Outline each blood parasite and name the species.
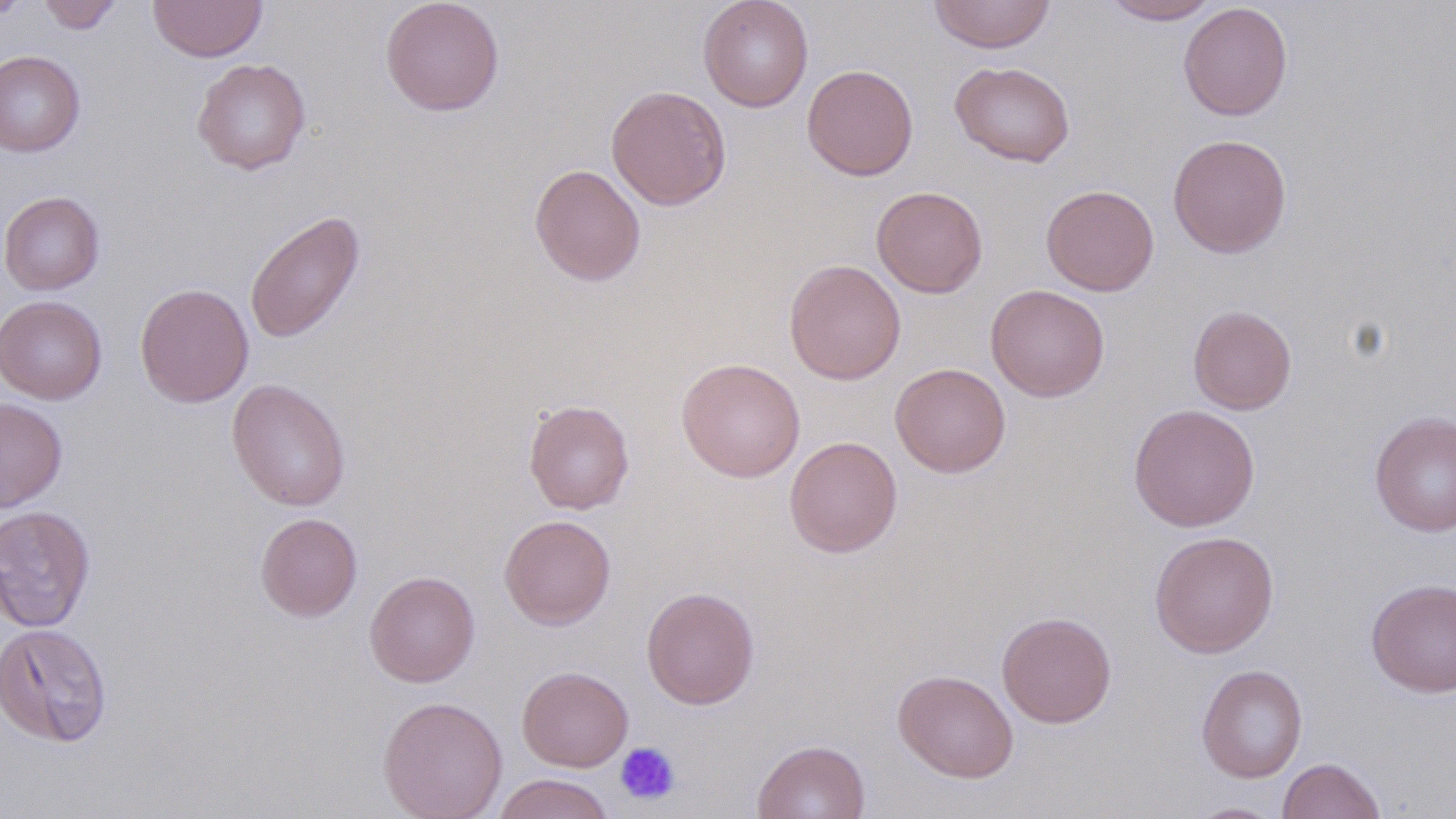

No blood parasites observed.

Approximate bounding boxes as named x1/y1/x2/y2 corners in pixels. Uninfected red blood cell locations: (x1=37, y1=0, x2=123, y2=33), (x1=149, y1=0, x2=267, y2=62), (x1=380, y1=0, x2=505, y2=116), (x1=697, y1=0, x2=814, y2=112), (x1=927, y1=0, x2=1056, y2=54), (x1=1101, y1=0, x2=1222, y2=24), (x1=1178, y1=3, x2=1294, y2=121), (x1=0, y1=51, x2=85, y2=157), (x1=192, y1=57, x2=311, y2=175), (x1=950, y1=61, x2=1076, y2=167), (x1=801, y1=64, x2=919, y2=181), (x1=605, y1=85, x2=732, y2=211), (x1=1167, y1=133, x2=1292, y2=258), (x1=530, y1=163, x2=646, y2=286), (x1=1041, y1=184, x2=1159, y2=296), (x1=871, y1=186, x2=988, y2=298), (x1=0, y1=191, x2=105, y2=295), (x1=244, y1=210, x2=365, y2=344), (x1=784, y1=259, x2=906, y2=385), (x1=134, y1=283, x2=254, y2=408), (x1=985, y1=284, x2=1110, y2=402), (x1=0, y1=294, x2=107, y2=404), (x1=1188, y1=304, x2=1297, y2=415), (x1=676, y1=357, x2=806, y2=482), (x1=890, y1=362, x2=1011, y2=478), (x1=227, y1=379, x2=351, y2=512), (x1=0, y1=397, x2=68, y2=512), (x1=523, y1=399, x2=634, y2=514), (x1=1128, y1=403, x2=1260, y2=531), (x1=1369, y1=410, x2=1456, y2=537), (x1=785, y1=435, x2=903, y2=558), (x1=0, y1=505, x2=96, y2=633), (x1=255, y1=512, x2=362, y2=622), (x1=499, y1=515, x2=616, y2=630), (x1=1149, y1=530, x2=1279, y2=658), (x1=364, y1=570, x2=480, y2=687), (x1=1366, y1=577, x2=1456, y2=697), (x1=641, y1=586, x2=760, y2=709), (x1=997, y1=611, x2=1116, y2=728), (x1=0, y1=622, x2=113, y2=747), (x1=1196, y1=664, x2=1307, y2=783), (x1=517, y1=665, x2=633, y2=771), (x1=893, y1=669, x2=1018, y2=783), (x1=378, y1=695, x2=508, y2=819), (x1=752, y1=739, x2=870, y2=819), (x1=1277, y1=757, x2=1386, y2=819), (x1=492, y1=773, x2=616, y2=819), (x1=1185, y1=801, x2=1285, y2=818). Platelet locations: (x1=614, y1=741, x2=681, y2=805). Slide-level diagnosis: no evidence of blood parasites. Light microscopy. May-Grünwald-Giemsa stain. Image is 1456×819 pixels. Captured at 1000x magnification. Single field of view. Thin blood smear.